Locate every malaria parasite.
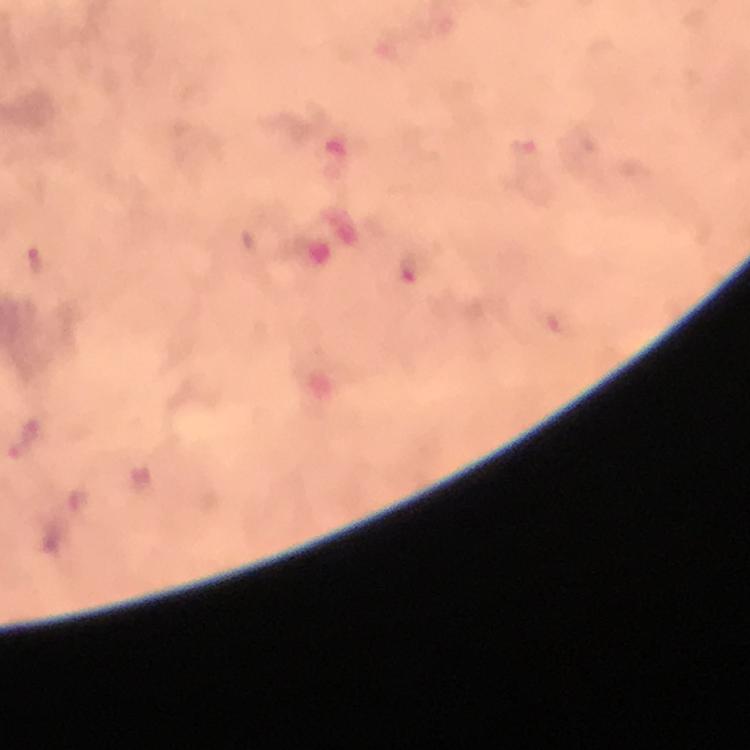

Approximate centers as {x, y} in pixels.
Malaria parasites: {38, 263}.

stain = Giemsa
magnification = 100x
cropped from = one field of view
preparation = thick blood smear
context = from a malaria diagnostic workup
image size = 750×750 pixels
immersion oil = applied
capture = smartphone camera through the microscope